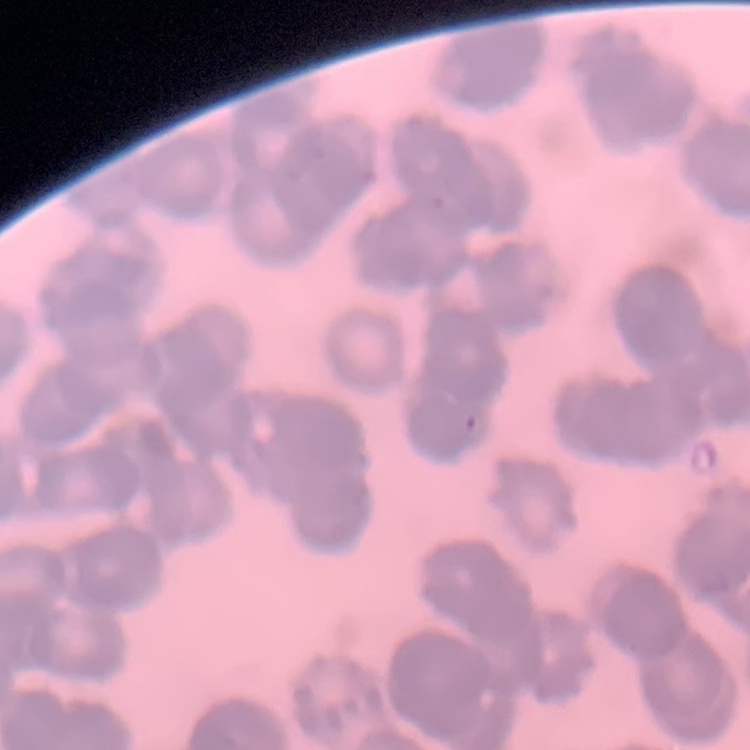
The erythrocytes show rouleaux formation. Square crop of a larger photomicrograph. Stained with either Field's or Giemsa. Thin blood smear.